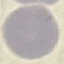

malaria status = uninfected
stain = Giemsa
capture = smartphone camera at the microscope eyepiece
preparation = thin blood smear
image type = automatically extracted cell patch, resized to 64 × 64 pixels